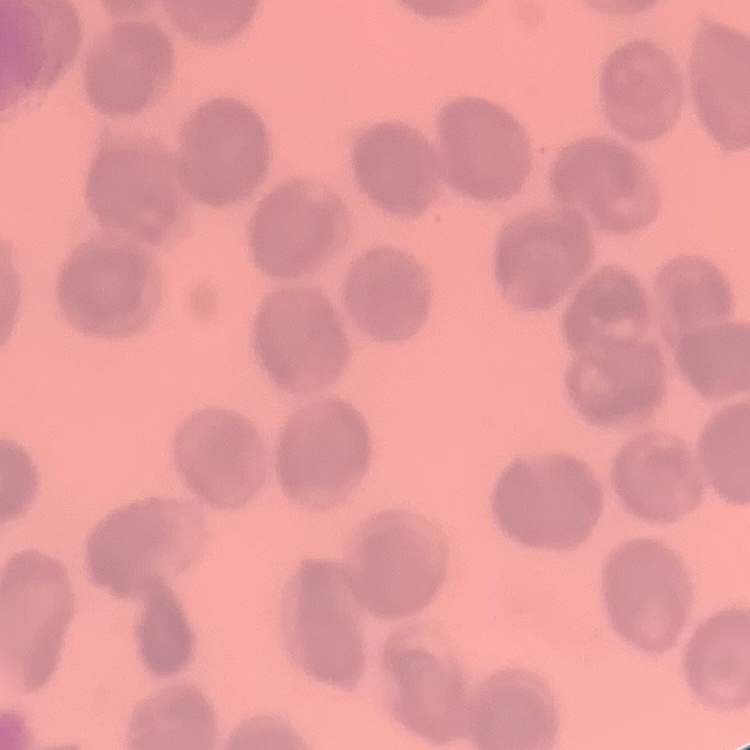 The erythrocytes exhibit no rouleaux formation. Thin peripheral smear. Stained with either Field's or Giemsa. Square crop of a larger photomicrograph.